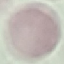

Summary:
  - Malaria status: uninfected
  - Image type: cell patch, automatically extracted from a larger field of view and resized to 64 × 64 pixels
  - Preparation: thin blood smear
  - Capture: smartphone through the microscope eyepiece
  - Stain: Giemsa